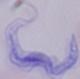
1000x magnification. Photomicrograph. A trypanosome is shown.